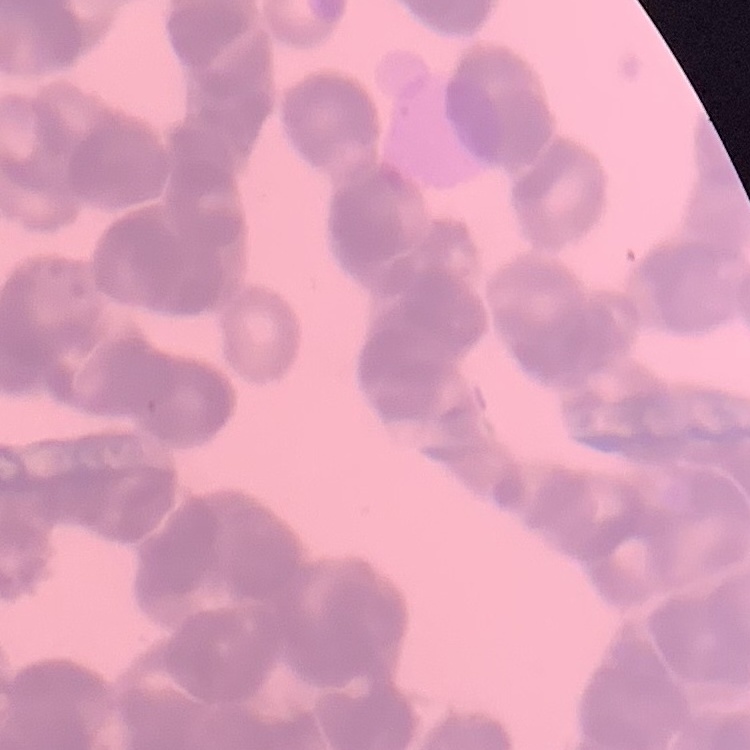
Summary:
  - Erythrocyte morphology: rouleaux formation
  - Image type: square crop of a larger photomicrograph
  - Stain: Field's or Giemsa
  - Preparation: thin blood film